Assess this cell for malaria.
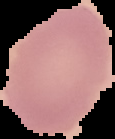
Uninfected.

From a thin blood smear. Image is 115×139 pixels. The area outside the segmented cell region is set to black.